Name the cell type shown.
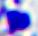

A leukocyte.

Summary:
  - Modality: photomicrograph
  - Magnification: 400x